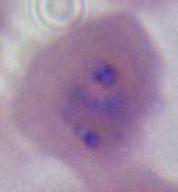
{
  "modality": "photomicrograph",
  "magnification": "400x or 1000x",
  "identification": "Plasmodium"
}